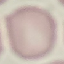

Result: no malaria parasites detected. Giemsa-stained preparation. Photographed with a smartphone camera at the microscope eyepiece. Automatically extracted cell patch, resized to 64 × 64 pixels. Thin smear of blood.